Identify the preparation type.
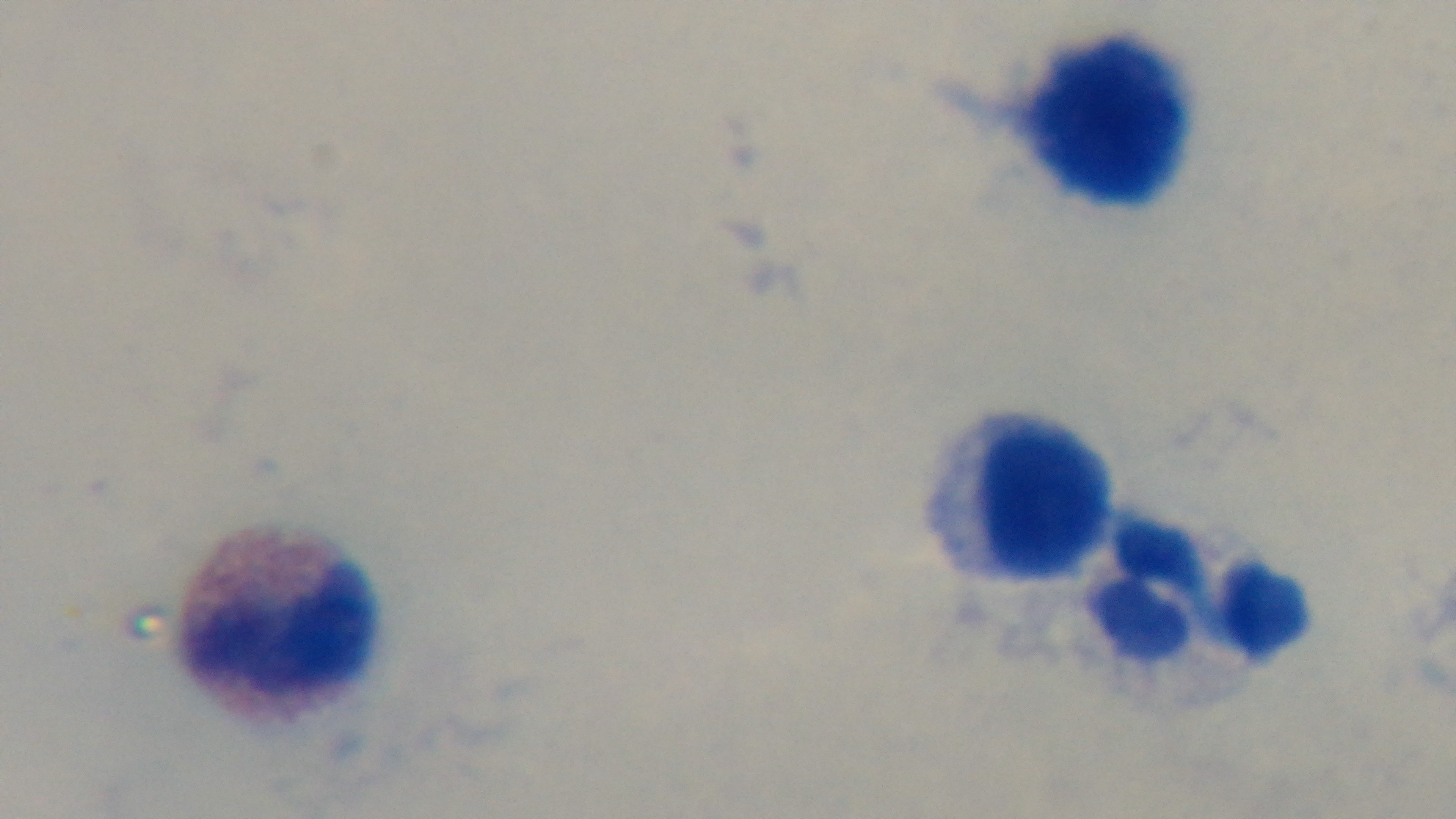

A thick smear.

Captured with a mounted 4K digital camera. Giemsa-stained. 100x oil-immersion objective. Single field of view. Malaria status: negative. Photomicrograph.